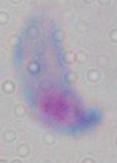
Summary:
  - Magnification: 1000x
  - Identification: Toxoplasma gondii
  - Modality: photomicrograph